Assess this cell for malaria.
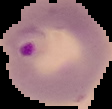

It is parasitized.

image size = 112×109 pixels
image type = cell region segmented out of the field of view; surrounding area masked to black
preparation = thin blood film